Name the blood parasite species.
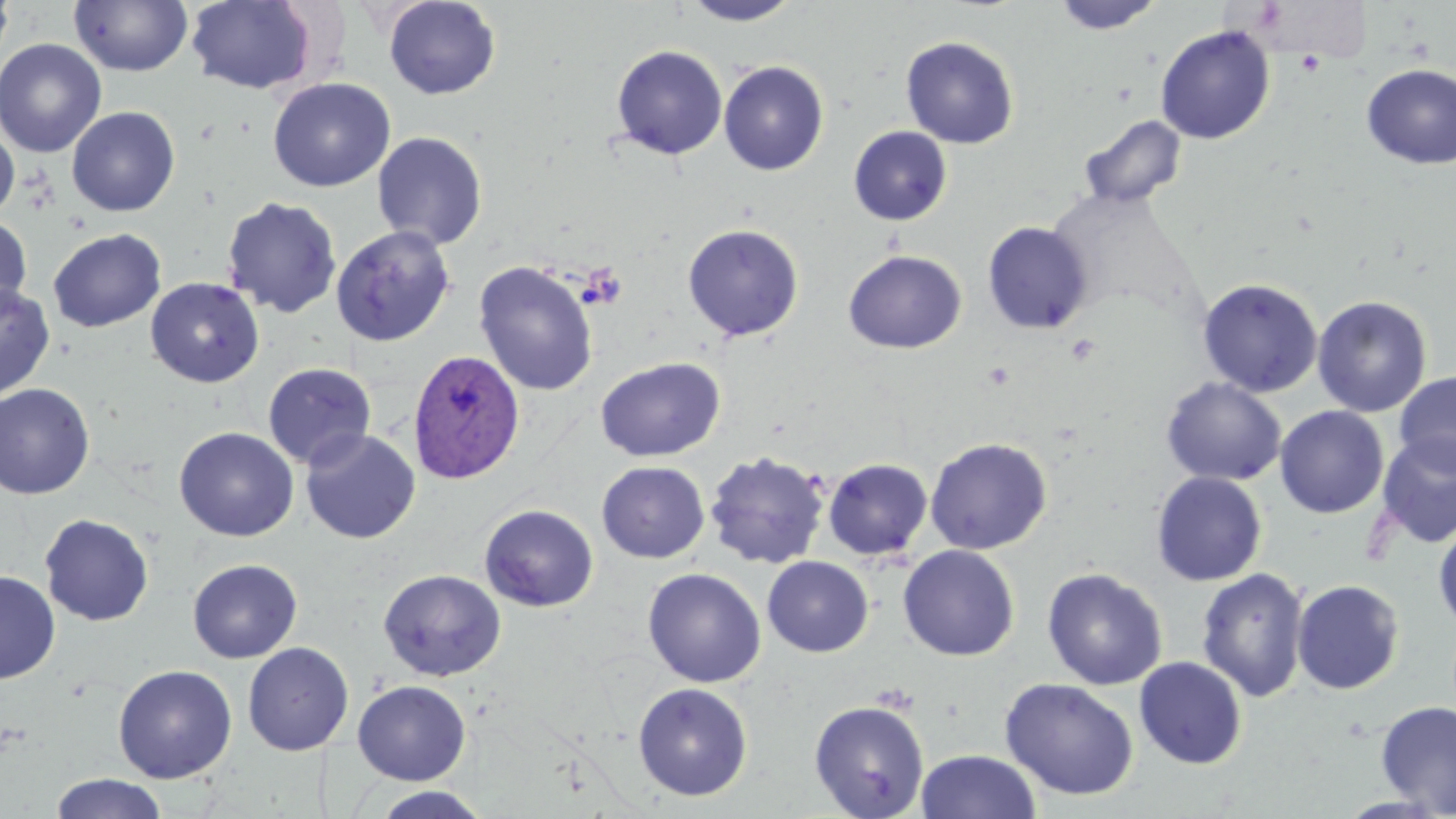

Plasmodium vivax.

image_size: 1456×819 pixels
modality: optical microscopy
preparation: thin blood film
plasmodium_vivax_infected_red_blood_cell_locations: 'approximate bounding boxes as (x1, y1, x2, y2) in pixels: (408, 349, 525, 485)'
platelet_locations: 'approximate bounding boxes as (x1, y1, x2, y2) in pixels: (1296, 51, 1325, 76), (1066, 333, 1101, 365)'
stain: May-Grünwald-Giemsa
uninfected_red_blood_cell_locations: 'approximate bounding boxes as (x1, y1, x2, y2) in pixels: (0, 0, 15, 68), (70, 0, 192, 77), (382, 0, 501, 100), (680, 0, 805, 26), (1052, 0, 1163, 35), (185, 1, 318, 94), (1155, 25, 1275, 144), (900, 36, 1019, 149), (0, 38, 107, 157), (610, 44, 728, 160), (718, 60, 829, 176), (1361, 64, 1456, 168), (268, 77, 395, 192), (66, 106, 180, 216), (1079, 114, 1187, 210), (0, 122, 19, 220), (848, 126, 953, 226), (371, 131, 488, 251), (222, 196, 342, 318), (0, 214, 32, 318), (982, 222, 1093, 334), (682, 223, 803, 342), (331, 225, 457, 346), (48, 228, 166, 332), (843, 249, 967, 353), (474, 261, 598, 396), (145, 277, 264, 388), (1197, 278, 1323, 397), (0, 282, 56, 402), (1312, 295, 1432, 417), (595, 356, 725, 462), (262, 362, 377, 470), (1394, 371, 1456, 476), (1161, 378, 1286, 486), (0, 383, 95, 499), (1275, 405, 1389, 518), (174, 427, 299, 541), (300, 429, 421, 544), (1375, 433, 1456, 549), (925, 437, 1052, 555), (704, 451, 830, 569), (822, 458, 933, 560), (596, 461, 709, 563), (1151, 471, 1267, 586), (479, 504, 598, 612), (39, 513, 154, 626), (1433, 519, 1456, 636), (898, 545, 1020, 661), (762, 556, 873, 657), (188, 558, 302, 663), (1196, 567, 1309, 703), (378, 568, 506, 681), (642, 568, 766, 688), (1042, 568, 1167, 690), (0, 571, 60, 683), (1292, 579, 1405, 695), (242, 642, 354, 756), (1134, 657, 1247, 769), (113, 664, 237, 783), (1000, 677, 1140, 801), (352, 680, 471, 785), (632, 682, 753, 801), (809, 699, 930, 818), (1375, 700, 1456, 816), (915, 749, 1042, 819), (50, 773, 169, 819), (369, 786, 493, 819)'
field_of_view: one of a larger specimen
magnification: 1000x